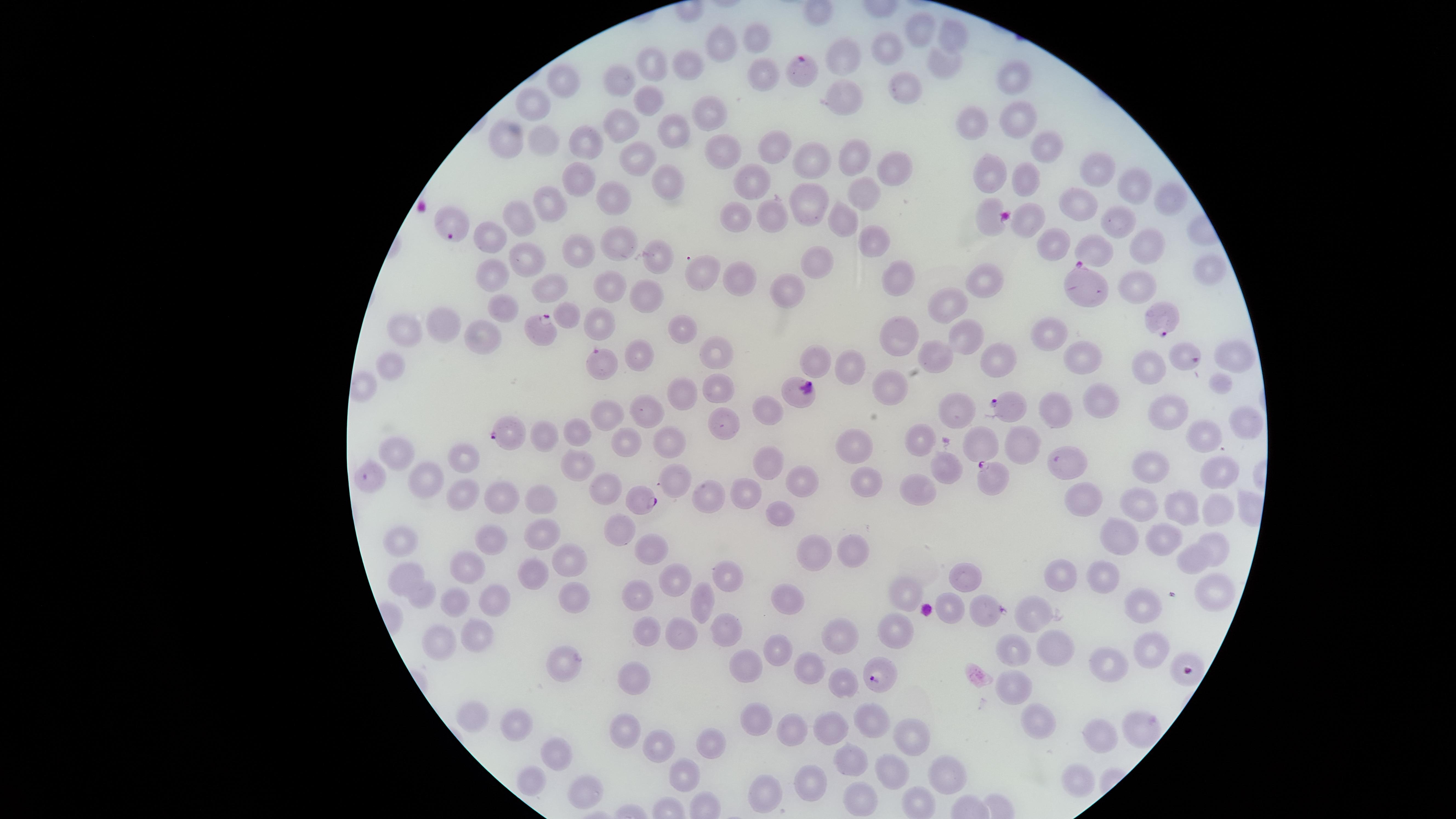
visible_region: circular
preparation: thin smear of blood
uninfected_RBCs: 'approximate marker points as {x, y} in pixels: {922, 29}, {951, 32}, {722, 36}, {756, 37}, {887, 51}, {846, 57}, {654, 60}, {942, 64}, {691, 65}, {767, 76}, {623, 77}, {1011, 80}, {563, 82}, {901, 88}, {845, 97}, {645, 100}, {531, 103}, {703, 112}, {1014, 115}, {621, 123}, {975, 123}, {671, 130}, {545, 138}, {590, 139}, {503, 141}, {1051, 143}, {776, 146}, {722, 149}, {640, 153}, {855, 160}, {808, 164}, {896, 167}, {1095, 171}, {991, 173}, {579, 178}, {1027, 179}, {663, 181}, {754, 181}, {1128, 184}, {867, 194}, {810, 196}, {613, 197}, {1172, 198}, {554, 202}, {1074, 202}, {842, 211}, {735, 213}, {775, 215}, {990, 217}, {1118, 218}, {516, 220}, {1027, 221}, {486, 238}, {872, 238}, {1150, 240}, {1050, 244}, {623, 245}, {1090, 249}, {579, 250}, {525, 255}, {660, 258}, {822, 262}, {739, 267}, {1208, 268}, {694, 272}, {899, 274}, {492, 275}, {610, 281}, {985, 281}, {1135, 283}, {788, 288}, {549, 289}, {649, 293}, {950, 305}, {502, 309}, {569, 313}, {443, 323}, {601, 324}, {404, 327}, {678, 327}, {903, 334}, {481, 335}, {964, 337}, {1051, 337}, {712, 350}, {936, 354}, {1081, 354}, {1236, 354}, {642, 357}, {1002, 358}, {820, 360}, {1145, 363}, {391, 365}, {853, 365}, {1219, 379}, {716, 387}, {895, 390}, {677, 392}, {1104, 396}, {954, 405}, {766, 409}, {645, 412}, {1056, 412}, {604, 415}, {1165, 415}, {1245, 423}, {724, 425}, {575, 428}, {546, 434}, {1207, 436}, {670, 437}, {983, 438}, {623, 439}, {919, 440}, {1021, 442}, {855, 445}, {398, 448}, {463, 453}, {769, 458}, {1070, 459}, {575, 461}, {1154, 464}, {941, 466}, {1216, 470}, {675, 479}, {802, 479}, {431, 485}, {611, 485}, {863, 486}, {744, 490}, {919, 490}, {464, 494}, {1085, 494}, {499, 497}, {1137, 497}, {710, 499}, {545, 502}, {1181, 502}, {783, 511}, {1217, 511}, {621, 526}, {1123, 535}, {490, 537}, {543, 537}, {1166, 539}, {404, 541}, {1220, 545}, {649, 547}, {857, 547}, {814, 551}, {570, 557}, {1193, 557}, {466, 564}, {539, 568}, {408, 576}, {674, 576}, {964, 576}, {726, 577}, {1102, 577}, {1057, 578}, {908, 585}, {637, 591}, {1214, 594}, {426, 595}, {576, 595}, {494, 596}, {701, 598}, {789, 599}, {456, 601}, {1143, 602}, {977, 607}, {950, 610}, {1034, 613}, {722, 627}, {646, 629}, {901, 629}, {680, 631}, {841, 633}, {478, 636}, {437, 644}, {1151, 645}, {1010, 649}, {778, 650}, {1059, 650}, {566, 661}, {809, 664}, {748, 665}, {1109, 668}, {630, 677}, {843, 682}, {1023, 683}, {477, 713}, {753, 720}, {517, 721}, {1037, 721}, {1143, 724}, {827, 725}, {872, 726}, {793, 728}, {623, 729}, {909, 733}, {1099, 735}, {713, 738}, {656, 743}, {561, 752}, {850, 758}, {687, 767}, {893, 771}, {947, 775}, {529, 777}, {1072, 782}, {808, 784}, {590, 789}, {766, 796}, {917, 800}, {862, 804}'
stain: Giemsa
parasitized_RBCs: 'approximate marker points as {x, y} in pixels: {801, 67}, {452, 223}, {1089, 293}, {1164, 317}, {545, 331}, {1187, 358}, {604, 363}, {800, 392}, {1003, 408}, {511, 432}, {368, 476}, {989, 478}, {644, 499}, {1189, 671}, {879, 674}'
capture: smartphone photograph through the microscope eyepiece
species: Plasmodium falciparum
image_size: 1456×819 pixels
field_of_view: single
presence: malaria parasites detected